Classify this cell by malaria status.
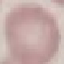

Uninfected.

preparation = thin blood film
stain = Giemsa
image type = automatically extracted cell patch, resized to 64 × 64 pixels
capture = smartphone through the microscope eyepiece